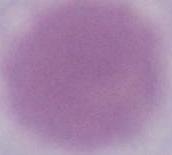
Summary:
  - Modality: photomicrograph
  - Magnification: 1000x
  - Identification: erythrocyte